State the preparation type.
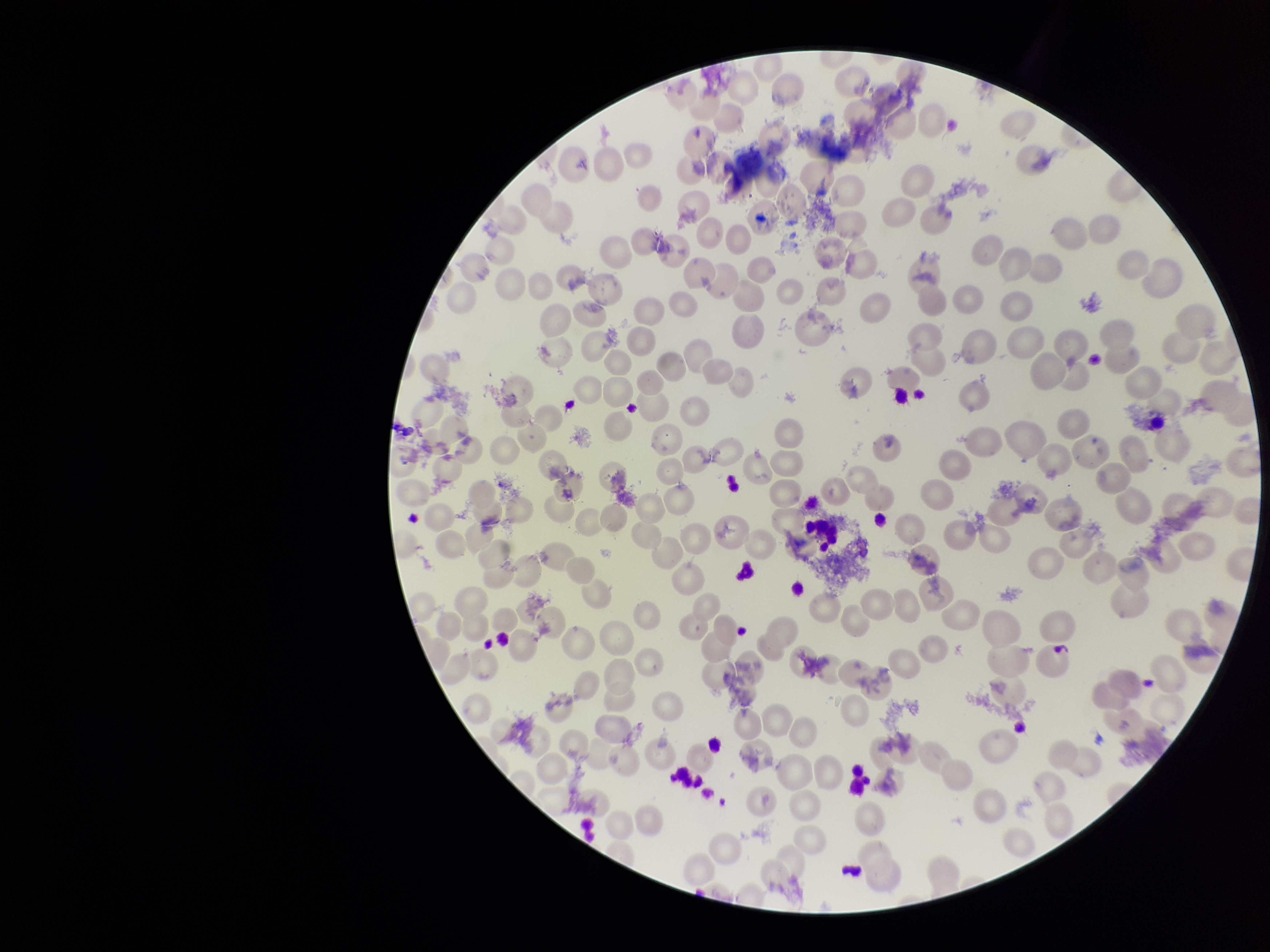
A thin smear.

Summary:
  - Red blood cell count: 156
  - Capture: smartphone photograph through the microscope eyepiece
  - Parasitized red blood cells: none detected
  - Stain: Giemsa
  - Patient malaria status: infected
  - Image size: 1270×952 pixels
  - Species reported for this patient: Plasmodium vivax
  - Field of view: single
  - Parasitized red blood cell count: 0